Classify this cell by malaria status.
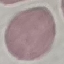

Uninfected.

Thin blood film. Cell patch, automatically extracted from a larger field of view and resized to 64 × 64 pixels. Giemsa stain. Acquired by smartphone through the microscope eyepiece.